Assess for Plasmodium parasites.
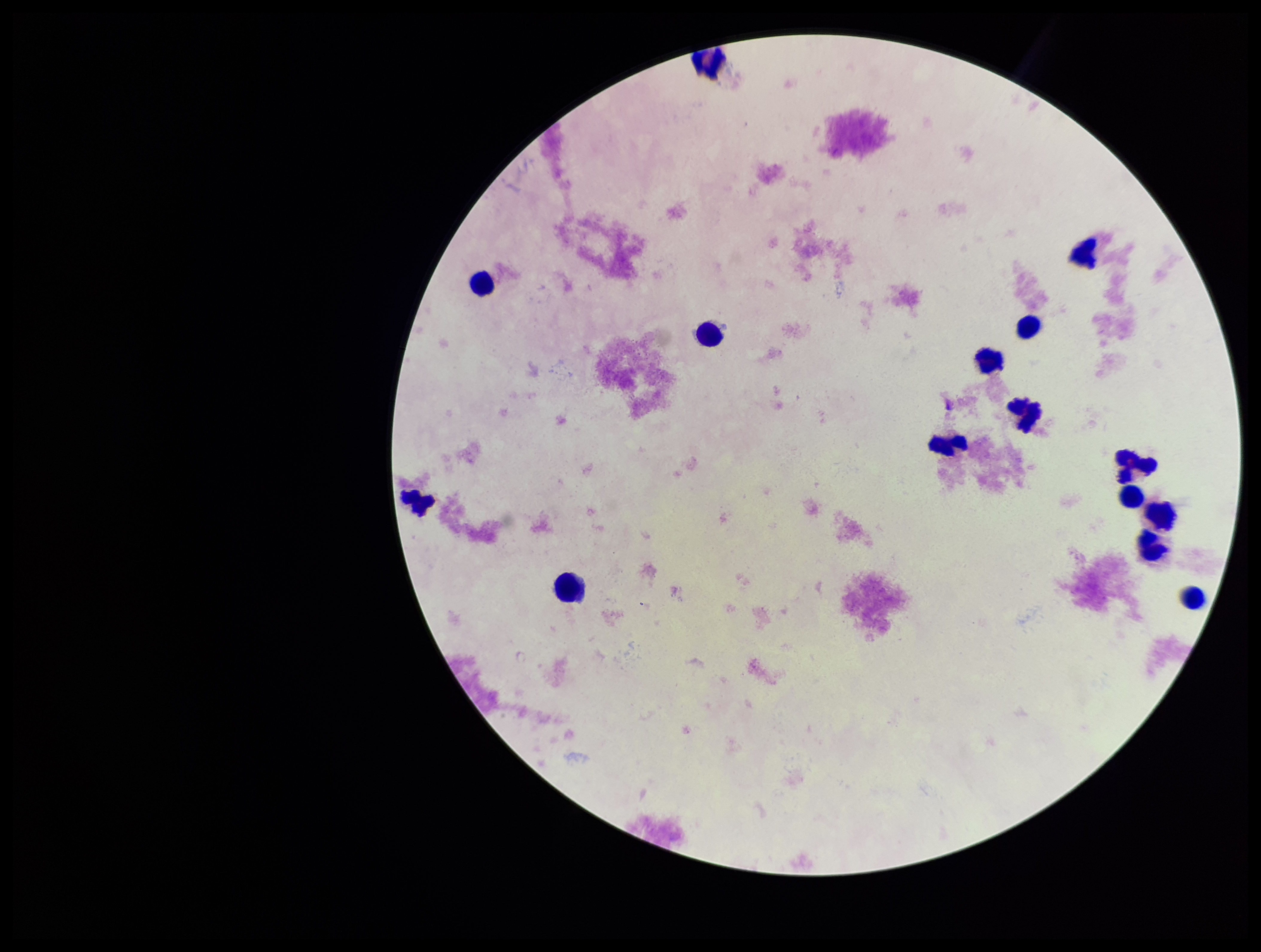
None identified.

stain = Giemsa
patient malaria status = negative
preparation = thick smear
field of view = one from this slide
parasite count = 0
capture = smartphone photograph through the microscope eyepiece
leukocyte count = 15
image size = 1261×952 pixels